Locate and identify every blood parasite.
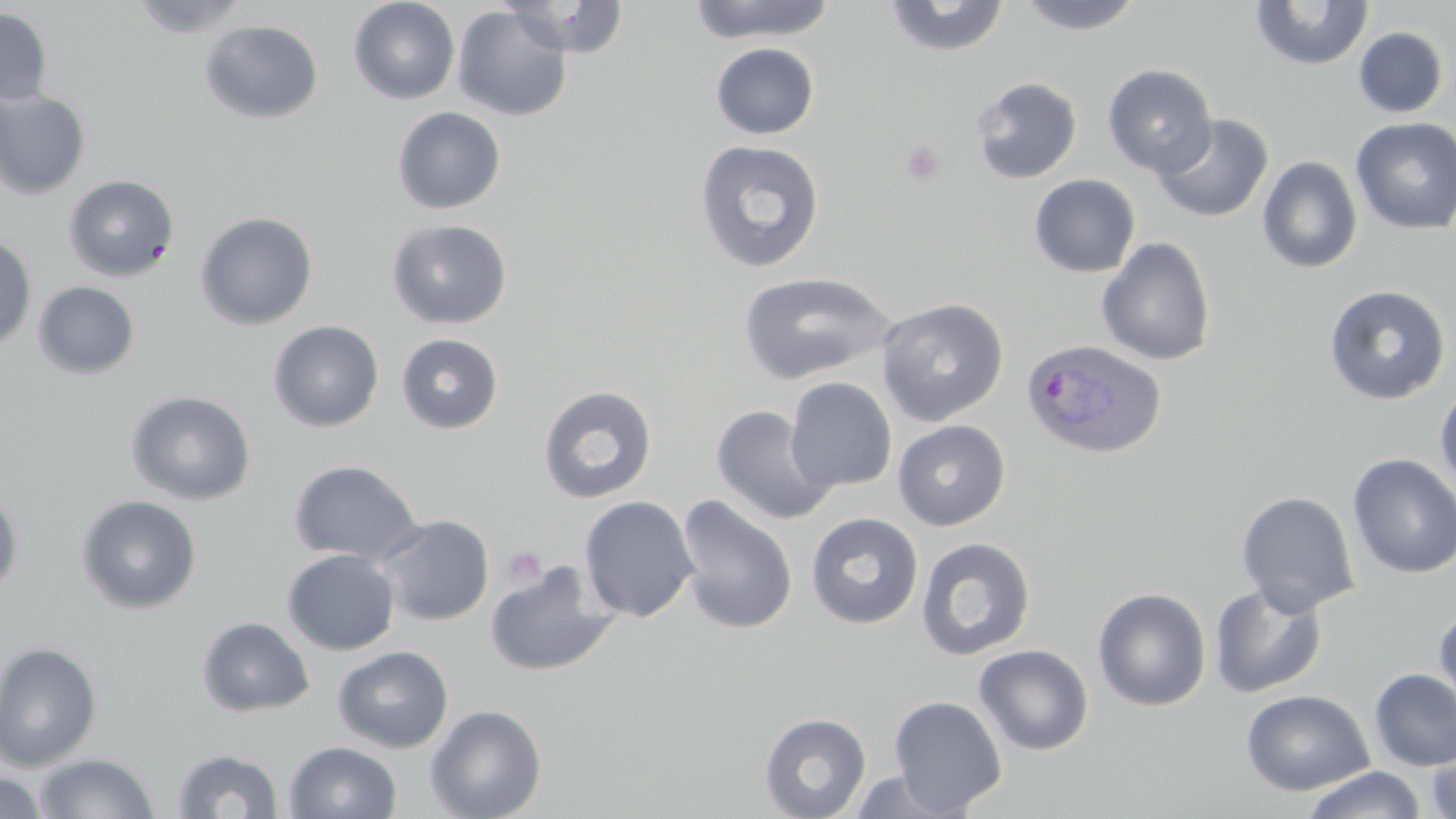
Approximate bounding boxes as [x1, y1, x2, y2] in pixels.
Plasmodium ovale-infected red blood cells: [1021, 338, 1167, 460].
No Plasmodium falciparum, Plasmodium malariae, Plasmodium vivax, Babesia divergens, or Trypanosoma brucei observed.

Summary:
  - Uninfected red blood cell locations: [129, 0, 253, 39], [348, 0, 460, 104], [686, 0, 838, 44], [883, 0, 1011, 58], [1015, 0, 1147, 35], [500, 1, 629, 57], [1249, 1, 1375, 71], [452, 5, 572, 121], [0, 7, 53, 106], [199, 20, 324, 124], [1353, 26, 1448, 118], [710, 42, 819, 139], [1102, 64, 1217, 177], [970, 77, 1083, 184], [0, 89, 91, 200], [392, 106, 506, 214], [1153, 113, 1274, 222], [1350, 117, 1456, 234], [695, 139, 825, 274], [1257, 156, 1363, 274], [63, 174, 179, 282], [1029, 174, 1140, 277], [194, 211, 318, 330], [386, 218, 513, 329], [0, 236, 37, 352], [1097, 237, 1216, 366], [738, 271, 895, 385], [32, 281, 140, 380], [1324, 284, 1450, 404], [876, 297, 1009, 426], [267, 320, 384, 432], [396, 333, 504, 434], [785, 377, 897, 492], [1434, 382, 1456, 494], [538, 385, 657, 504], [126, 390, 256, 505], [711, 404, 838, 525], [892, 419, 1010, 531], [1347, 453, 1456, 579], [288, 459, 423, 565], [0, 489, 23, 600], [1236, 491, 1360, 616], [675, 494, 799, 635], [76, 495, 202, 614], [579, 496, 699, 622], [805, 513, 924, 629], [376, 514, 494, 626], [915, 536, 1036, 661], [282, 548, 400, 655], [483, 559, 621, 678], [1209, 581, 1328, 698], [1093, 587, 1211, 711], [1433, 603, 1456, 715], [196, 616, 315, 717], [0, 641, 102, 772], [974, 644, 1094, 755], [332, 645, 454, 753], [1369, 668, 1456, 772], [1240, 689, 1374, 796], [889, 695, 1007, 815], [425, 704, 547, 819], [760, 711, 872, 818], [1425, 736, 1456, 819], [285, 741, 402, 819], [171, 747, 284, 818], [34, 752, 158, 818], [1300, 766, 1427, 819], [847, 769, 962, 818], [1, 771, 47, 819]
  - Platelet locations: [901, 141, 944, 185], [503, 547, 547, 587]
  - Slide-level diagnosis: Plasmodium ovale
  - Stain: May-Grünwald-Giemsa
  - Field of view: single
  - Preparation: thin blood film
  - Magnification: 1000x
  - Modality: optical microscopy
  - Image size: 1456×819 pixels